Report the malaria status of this cell.
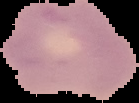

Uninfected.

Summary:
  - Image type: segmented cell region on a black background
  - Image size: 139×103 pixels
  - Preparation: thin blood film